Assess this cell for malaria.
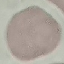
Uninfected.

Thin blood film. Photographed with a smartphone camera at the microscope eyepiece. Giemsa-stained preparation. Cell patch, automatically extracted from a larger field of view and resized to 64 × 64 pixels.